State the blood parasite species.
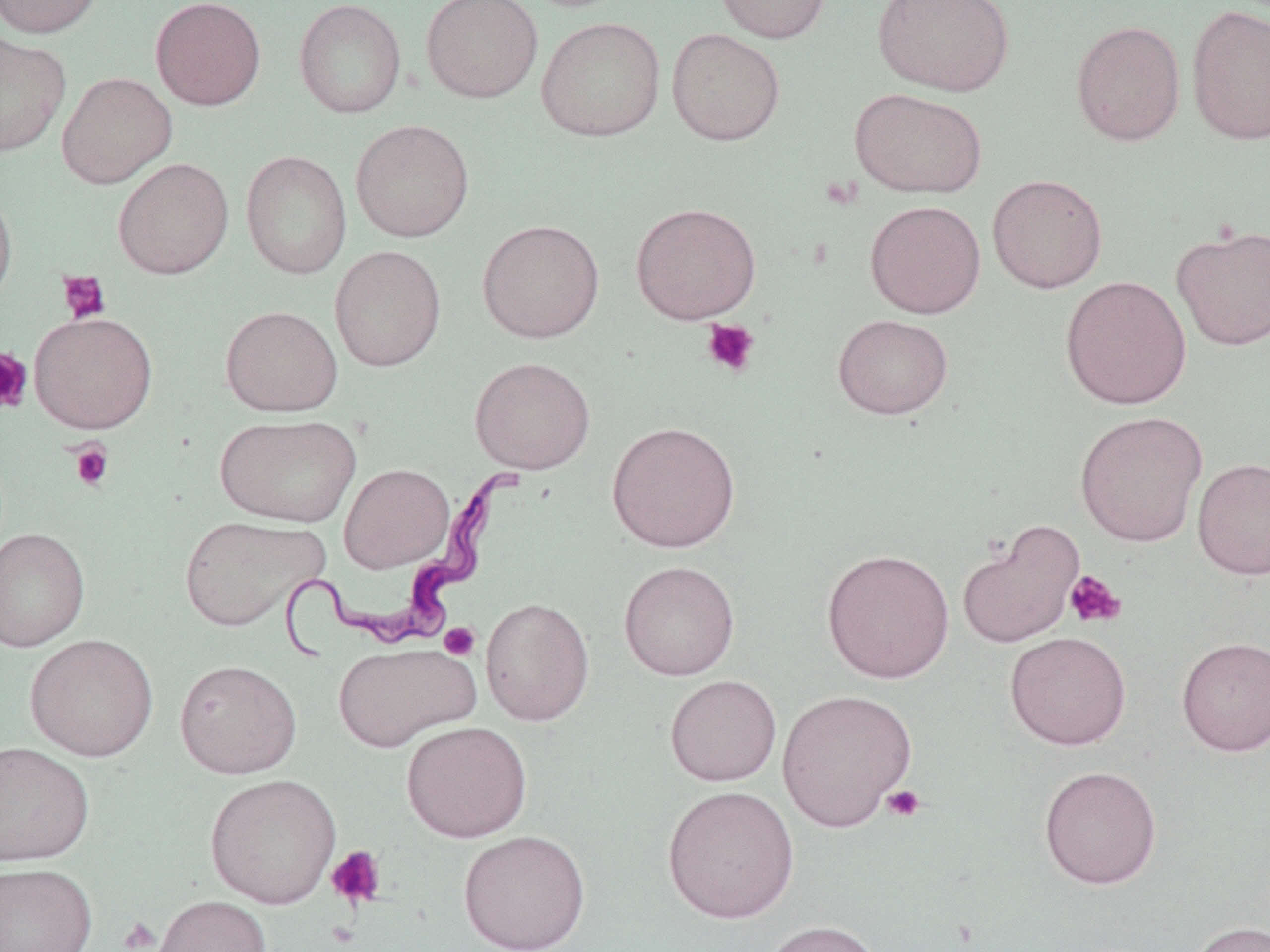

Trypanosoma brucei.

field of view = one of a larger specimen
stain = May-Grünwald-Giemsa
uninfected red blood cell locations (subset) = approximate bounding boxes as [x1, y1, x2, y2] in pixels: [0, 0, 104, 38], [150, 0, 266, 110], [294, 0, 406, 118], [420, 0, 543, 103], [714, 0, 831, 44], [872, 0, 1014, 97], [1185, 5, 1270, 145], [535, 17, 666, 141], [1071, 20, 1186, 146], [666, 28, 786, 145], [0, 31, 71, 157], [56, 72, 177, 189], [849, 88, 988, 199], [350, 119, 474, 242], [241, 149, 352, 280], [112, 157, 234, 279], [986, 174, 1108, 293], [0, 182, 18, 311], [864, 200, 986, 319], [477, 219, 604, 343], [1170, 223, 1270, 351], [329, 245, 446, 372], [1059, 275, 1192, 410], [220, 305, 342, 416], [29, 312, 158, 433], [832, 314, 953, 419], [470, 356, 595, 474], [1074, 410, 1208, 548], [215, 414, 361, 527], [606, 421, 741, 554], [1192, 457, 1270, 580], [339, 463, 454, 573], [179, 514, 327, 631], [0, 527, 90, 652], [821, 548, 955, 684], [618, 560, 740, 681], [480, 597, 595, 726], [1005, 631, 1130, 750], [24, 633, 159, 762], [1176, 636, 1270, 756], [333, 641, 481, 752], [174, 659, 301, 778], [664, 674, 781, 786], [776, 688, 917, 831], [400, 720, 533, 843], [0, 741, 95, 866], [1039, 765, 1162, 889], [204, 774, 342, 909], [661, 785, 800, 923], [457, 829, 591, 951], [0, 862, 97, 952], [151, 895, 272, 952], [759, 919, 885, 952], [1186, 919, 1269, 952]
Trypanosoma brucei locations = approximate bounding boxes as [x1, y1, x2, y2] in pixels: [270, 468, 525, 660]
magnification = 1000x
image size = 1270×952 pixels
modality = optical microscopy
platelet locations (subset) = approximate bounding boxes as [x1, y1, x2, y2] in pixels: [57, 269, 111, 324], [701, 319, 760, 378], [0, 348, 33, 415], [69, 441, 114, 492], [1064, 570, 1126, 628], [439, 622, 481, 661], [882, 785, 925, 823], [326, 845, 386, 909], [117, 917, 160, 951]
preparation = thin blood smear